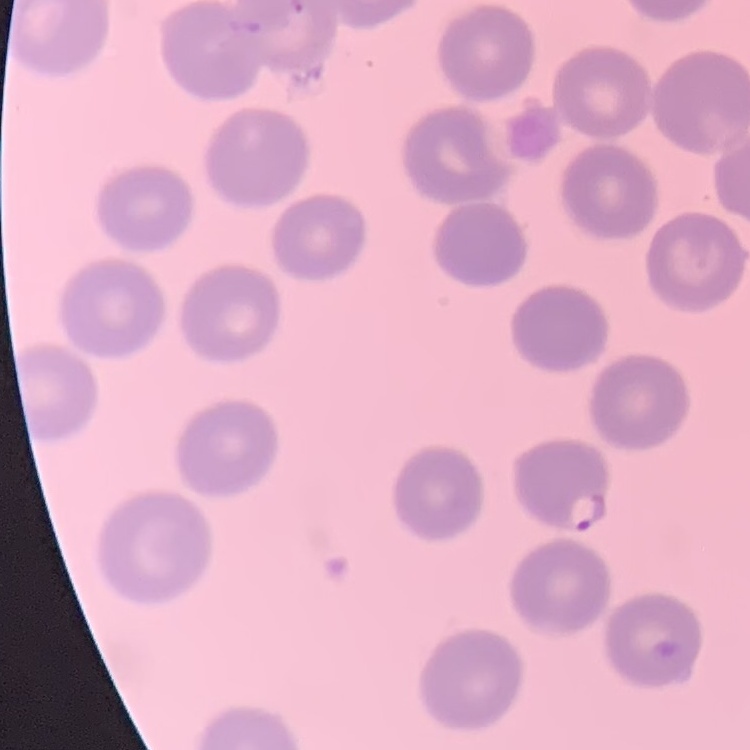
{
  "erythrocyte_morphology": "no rouleaux formation",
  "image_type": "one tile cut from a larger photomicrograph",
  "preparation": "thin blood film",
  "stain": "Field's or Giemsa"
}